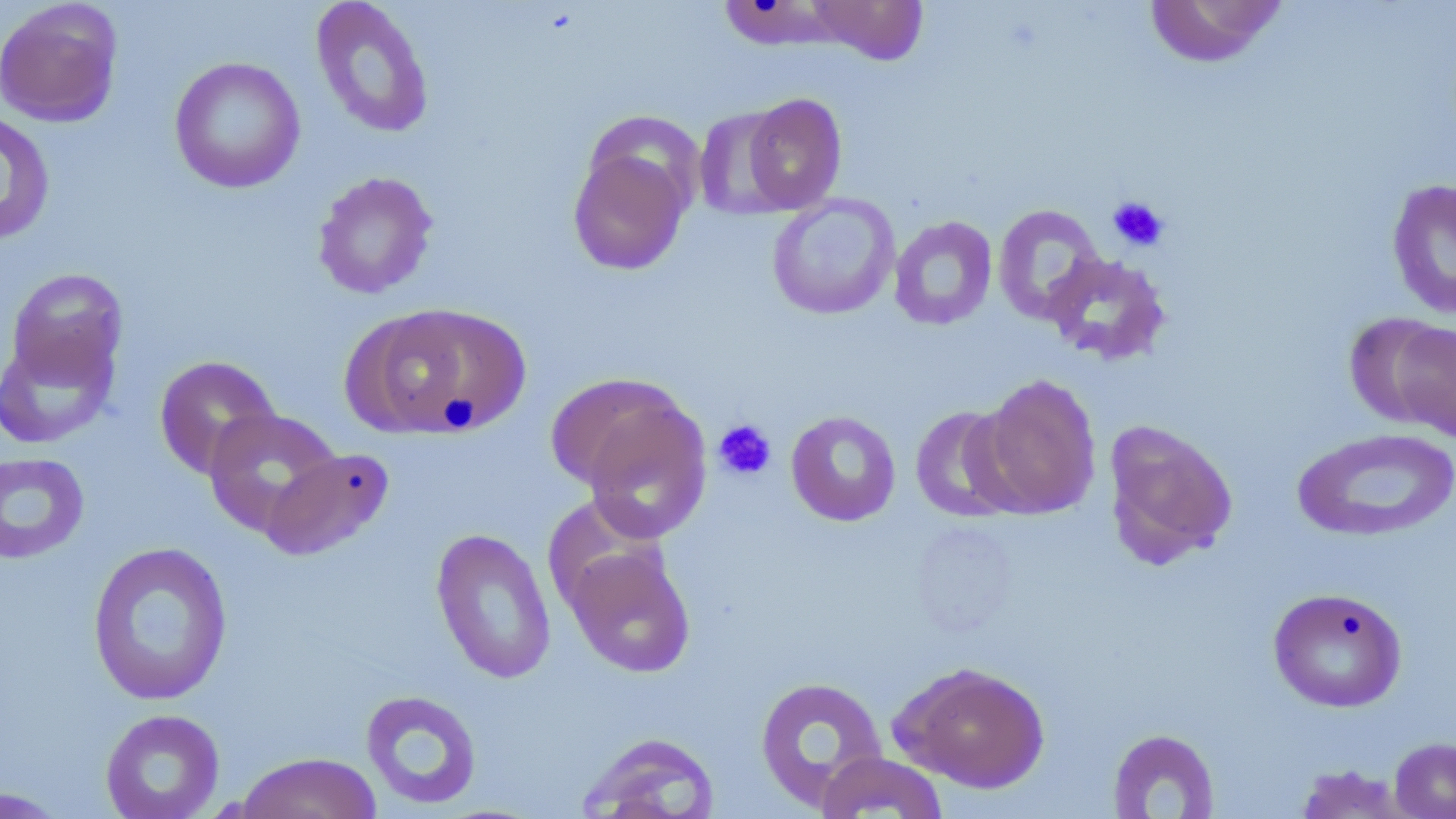

{
  "slide_level_diagnosis": "no evidence of blood parasites",
  "modality": "light microscopy",
  "magnification": "1000x",
  "stain": "May-Grünwald-Giemsa",
  "image_size": "1456×819 pixels",
  "uninfected_red_blood_cell_locations": "approximate bounding boxes as (x1, y1, x2, y2) in pixels: (806, 0, 929, 65), (1143, 0, 1288, 68), (0, 1, 124, 128), (310, 1, 434, 139), (721, 2, 828, 56), (168, 56, 306, 194), (740, 93, 847, 214), (693, 107, 798, 220), (0, 110, 56, 246), (567, 142, 694, 275), (312, 171, 438, 300), (1386, 177, 1456, 319), (767, 194, 901, 320), (992, 204, 1106, 325), (889, 216, 998, 331), (1042, 253, 1172, 366), (5, 267, 129, 390), (349, 304, 528, 438), (1346, 313, 1456, 435), (0, 327, 119, 450), (153, 354, 282, 479), (547, 371, 695, 498), (976, 373, 1101, 518), (577, 398, 713, 542), (909, 405, 1027, 523), (202, 407, 343, 538), (785, 409, 901, 526), (1102, 419, 1239, 569), (1292, 427, 1455, 542), (261, 447, 395, 562), (0, 452, 91, 565), (431, 527, 557, 685), (86, 540, 234, 706), (563, 543, 696, 678), (1268, 586, 1407, 712), (891, 660, 1051, 793), (754, 675, 888, 809), (360, 689, 483, 810), (100, 709, 225, 819), (1107, 728, 1220, 818), (579, 731, 721, 819), (1389, 736, 1456, 818), (814, 751, 950, 818), (235, 752, 382, 819), (1293, 763, 1415, 819), (0, 786, 70, 818)",
  "field_of_view": "single",
  "preparation": "thin blood smear",
  "platelet_locations": "approximate bounding boxes as (x1, y1, x2, y2) in pixels: (1107, 195, 1170, 252), (713, 418, 777, 481)"
}